Comment on the morphology of the red blood cells.
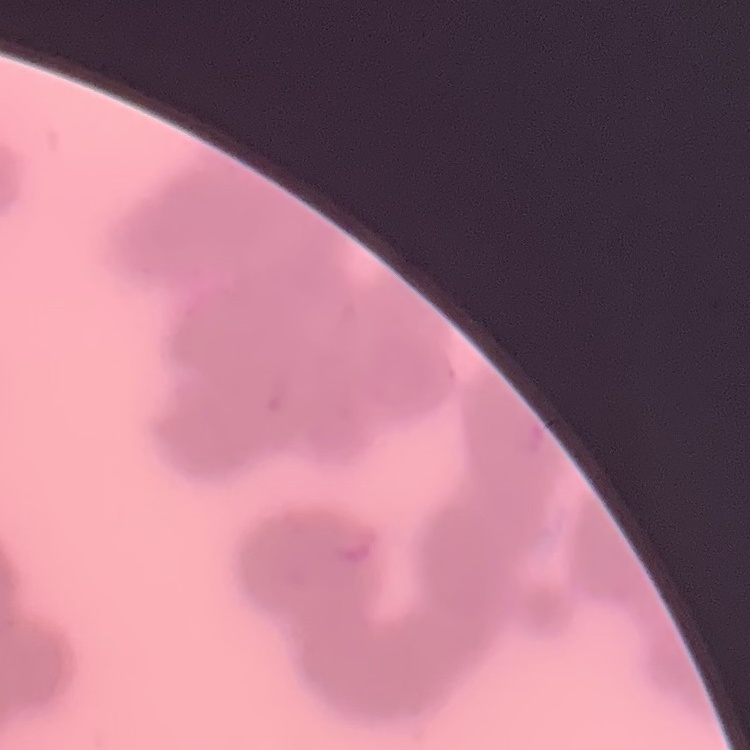

They show rouleaux formation.

Thin blood film. One tile cut from a larger photomicrograph. Field's or Giemsa stain.